Identify the blood parasite species.
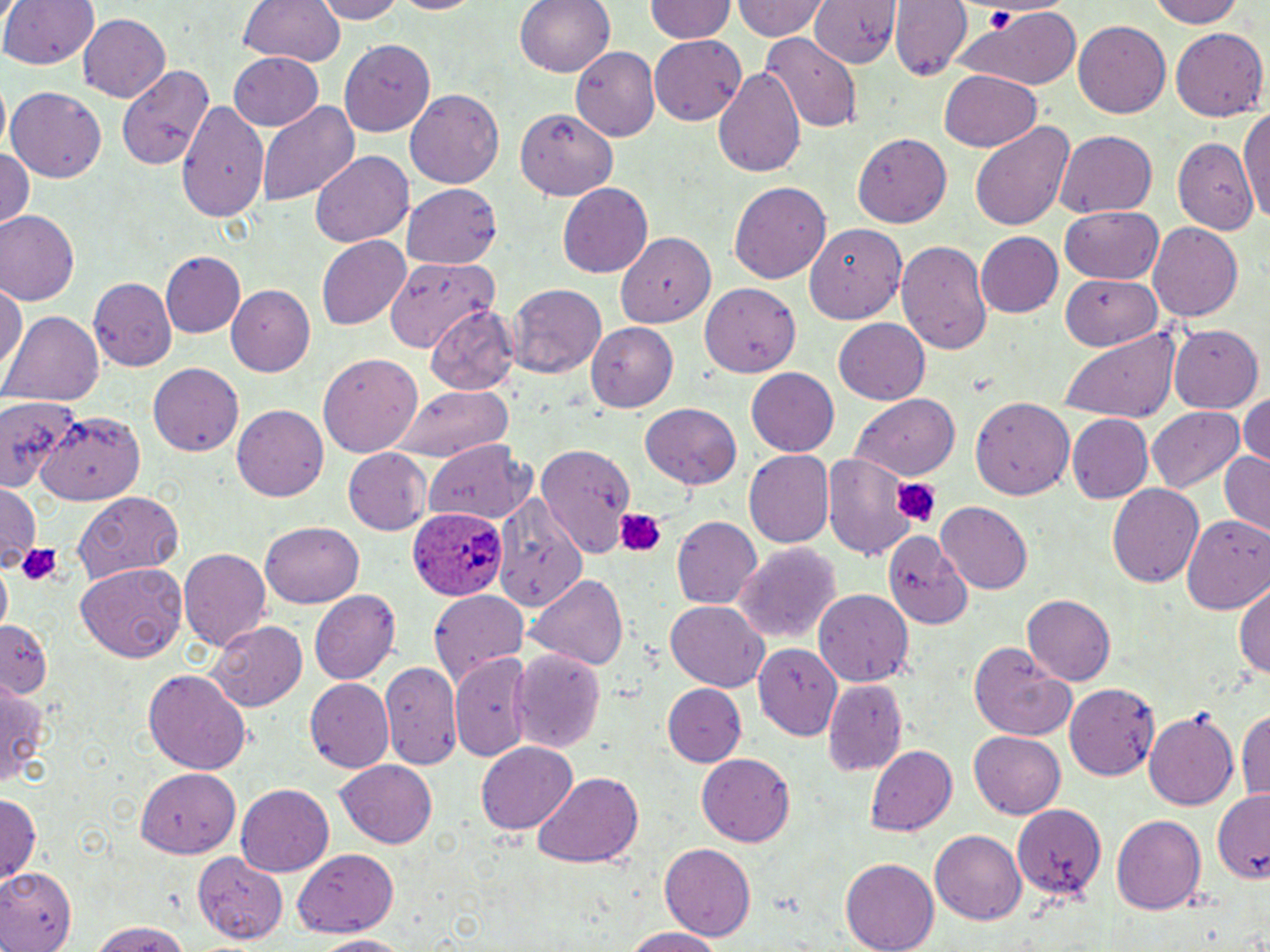

Plasmodium ovale.

Approximate bounding boxes as (x1, y1, x2, y2) in pixels. Uninfected red blood cell locations: (7, 0, 96, 73), (235, 0, 345, 67), (310, 0, 407, 24), (384, 0, 488, 17), (515, 0, 615, 78), (645, 0, 734, 43), (734, 0, 828, 43), (891, 0, 971, 80), (1152, 0, 1245, 28), (809, 2, 896, 70), (955, 10, 1084, 90), (75, 12, 169, 105), (1074, 18, 1171, 117), (1171, 29, 1267, 122), (761, 34, 863, 133), (649, 37, 745, 124), (340, 39, 434, 136), (570, 47, 658, 139), (228, 50, 324, 131), (119, 60, 218, 173), (712, 66, 807, 180), (938, 70, 1041, 152), (8, 87, 107, 182), (405, 90, 503, 191), (257, 99, 358, 208), (177, 100, 273, 221), (517, 106, 617, 201), (1242, 107, 1270, 224), (969, 121, 1075, 233), (1055, 128, 1156, 216), (853, 131, 949, 228), (1172, 136, 1256, 233), (0, 145, 36, 233), (311, 152, 414, 247), (730, 180, 830, 285), (402, 183, 503, 266), (559, 183, 654, 279), (1058, 206, 1163, 283), (1, 211, 80, 304), (805, 220, 906, 325), (1148, 222, 1243, 321), (617, 228, 717, 331), (976, 232, 1064, 317), (317, 236, 410, 329), (896, 239, 994, 358), (159, 250, 245, 339), (384, 258, 497, 352), (1060, 275, 1163, 349), (90, 278, 175, 369), (0, 281, 26, 378), (226, 283, 315, 376), (702, 283, 801, 373), (507, 287, 605, 375), (424, 303, 520, 396), (6, 312, 102, 407), (832, 319, 930, 405), (586, 321, 680, 415), (1168, 326, 1262, 415), (1057, 328, 1182, 424), (318, 352, 423, 454), (149, 363, 243, 459), (745, 368, 842, 458), (387, 384, 515, 459), (1238, 392, 1270, 467), (0, 393, 83, 491), (851, 394, 962, 480), (971, 396, 1075, 500), (640, 403, 743, 490), (232, 405, 329, 501), (1150, 407, 1246, 493), (38, 411, 144, 506), (1067, 416, 1152, 501), (425, 439, 535, 526), (536, 443, 631, 557), (344, 448, 432, 535), (743, 448, 833, 547), (1218, 449, 1270, 539), (823, 454, 920, 559), (0, 483, 39, 566), (1107, 483, 1203, 591), (490, 487, 590, 613), (75, 490, 185, 582), (936, 501, 1032, 595), (1183, 513, 1270, 613), (674, 516, 762, 611), (257, 522, 362, 609), (881, 529, 970, 627), (734, 542, 840, 646), (180, 549, 270, 652), (76, 562, 187, 663), (527, 571, 628, 671), (1234, 576, 1270, 686), (814, 588, 913, 687), (310, 589, 402, 685), (431, 591, 528, 687), (1023, 595, 1116, 686), (664, 601, 768, 692), (208, 618, 308, 712), (0, 619, 54, 699), (967, 639, 1079, 742), (754, 644, 844, 741), (509, 648, 606, 754), (452, 655, 537, 759), (379, 658, 464, 768), (143, 668, 253, 774), (823, 677, 908, 776), (304, 678, 393, 773), (1064, 681, 1162, 780), (662, 683, 746, 765), (0, 684, 45, 784), (1239, 702, 1270, 805), (1143, 709, 1240, 809), (968, 731, 1066, 818), (477, 742, 578, 834), (866, 744, 957, 838), (699, 752, 797, 845), (336, 759, 437, 849), (136, 766, 240, 856), (532, 772, 644, 869), (236, 783, 334, 875), (1213, 791, 1270, 884), (0, 793, 40, 884), (1013, 804, 1105, 898), (1112, 814, 1208, 915), (931, 828, 1027, 925), (661, 843, 755, 940), (290, 847, 398, 937), (196, 853, 289, 943), (841, 859, 940, 952), (0, 866, 77, 952), (85, 920, 195, 951), (621, 926, 730, 952), (309, 934, 416, 950). Plasmodium ovale-infected red blood cell locations: (409, 508, 503, 601). Platelet locations: (982, 5, 1016, 29), (888, 474, 942, 528), (613, 507, 667, 557), (18, 541, 62, 588). Thin blood smear. Optical microscopy. May-Grünwald-Giemsa stain. Captured at 1000x magnification. Image is 1270×952 pixels. Single field of view.